Identify the preparation type.
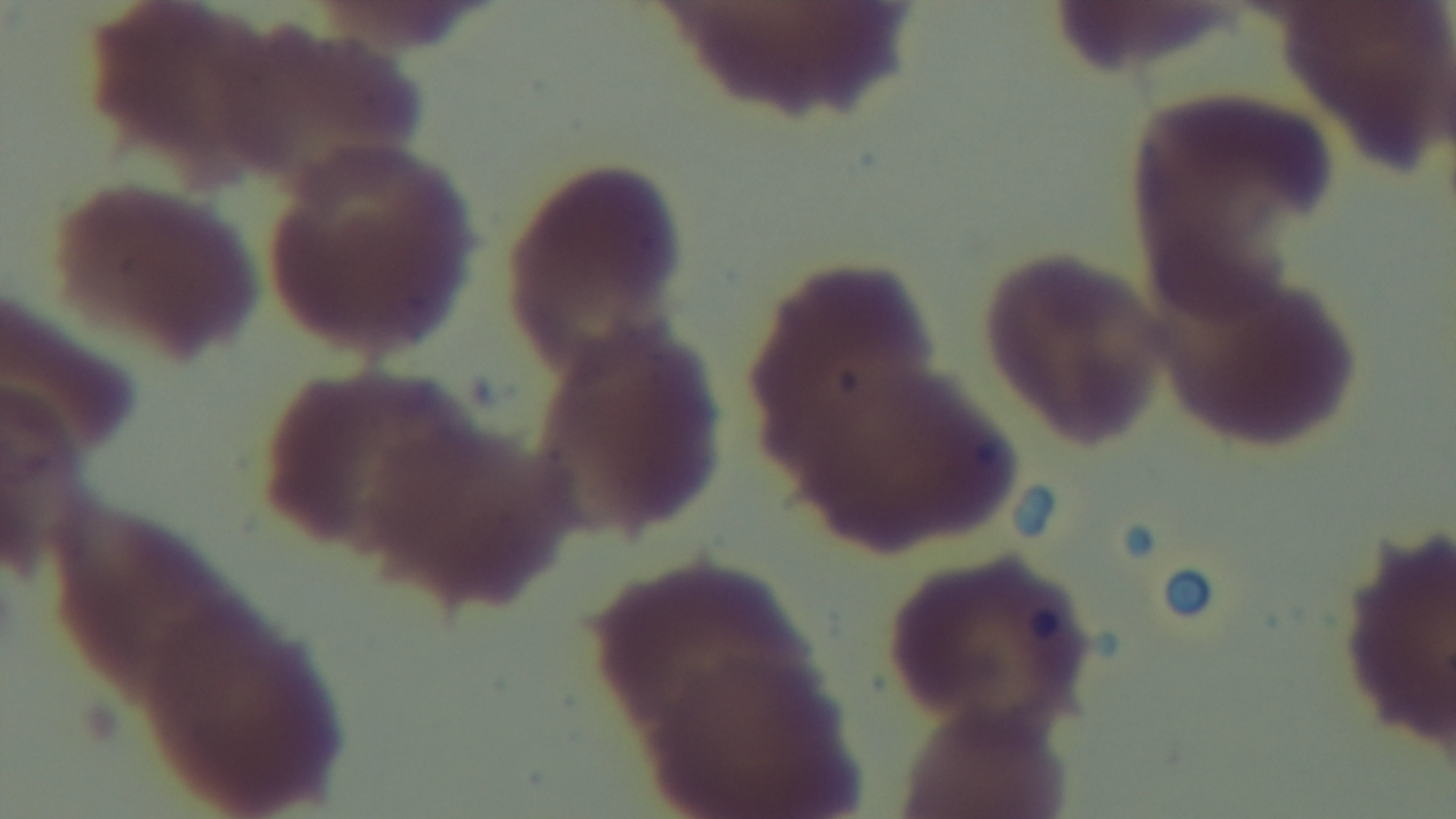

It is a thin blood film.

Malaria status: negative. Photomicrograph. Oil-immersion objective, 100x. Mounted 4K digital camera. Giemsa stain. One field from the slide.